Locate every Plasmodium parasite.
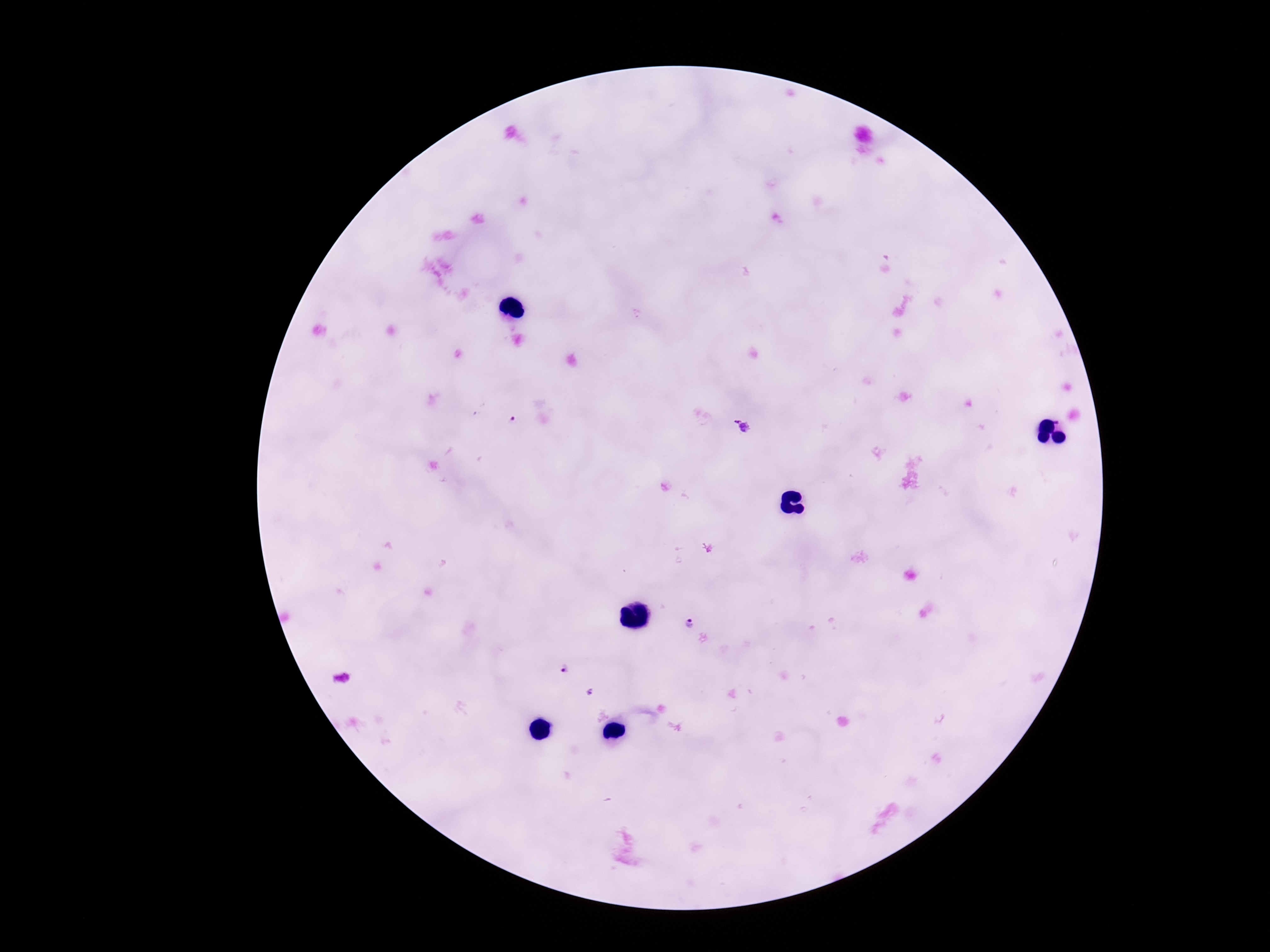

Approximate centers as {x, y} in pixels.
Plasmodium parasites: {513, 420}, {742, 427}, {687, 623}, {566, 667}.

Image is 1270×952 pixels. One field from this slide. Photographed through the microscope eyepiece with a smartphone camera. Giemsa-stained preparation. 100x magnification. Thick peripheral-blood smear. Patient malaria status: positive.